Report the malaria status of this cell.
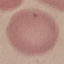
Uninfected.

Photographed with a smartphone camera at the microscope eyepiece. Giemsa-stained preparation. Automatically extracted cell patch, resized to 64 × 64 pixels. Thin blood film.